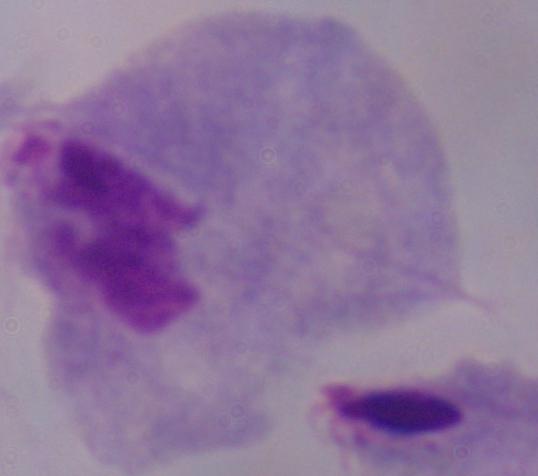
identification = trichomonad
modality = micrograph
magnification = 1000x